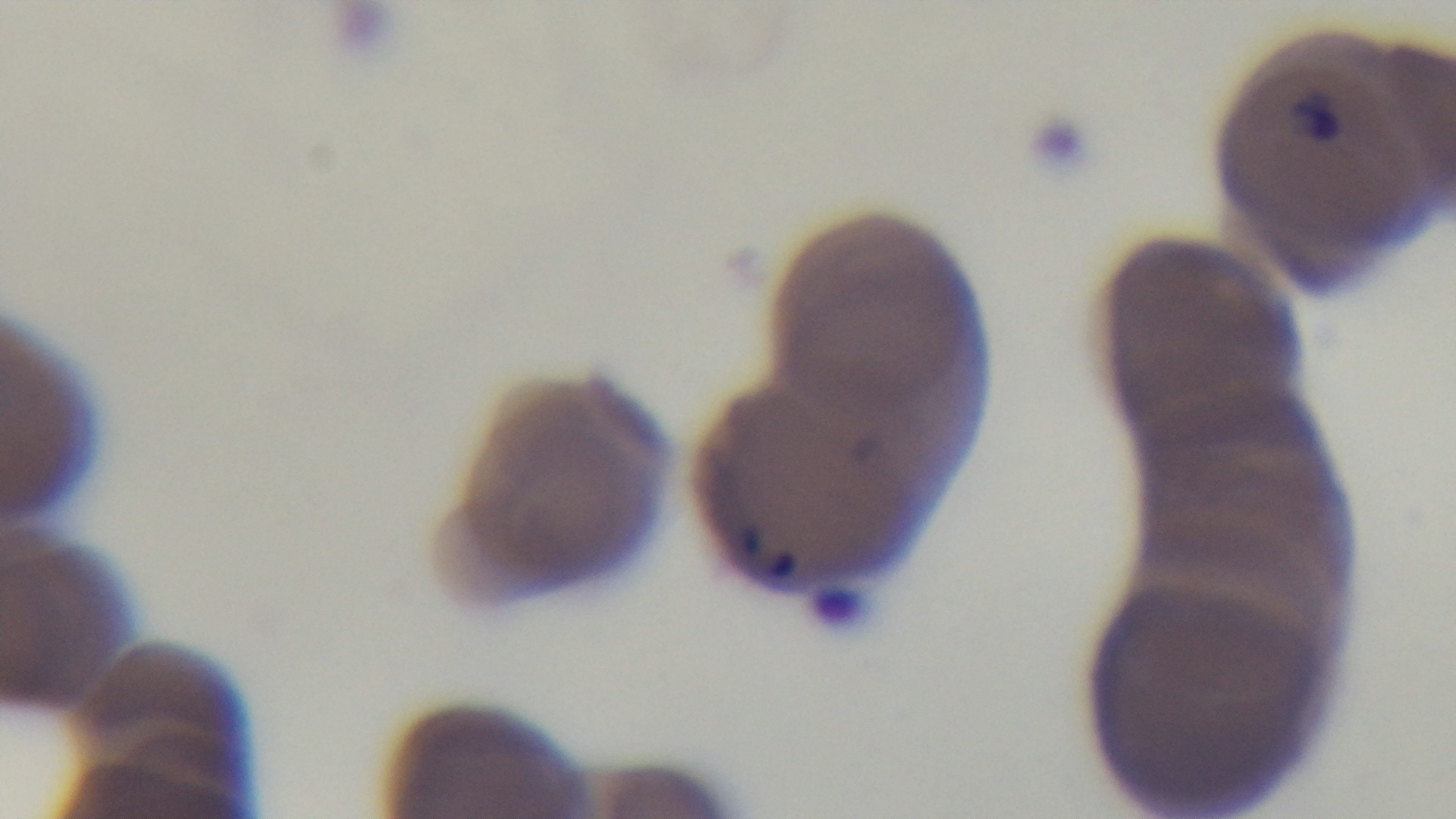

Malaria status: positive. 100x oil-immersion objective. Single field of view. Preparation: thin blood film. Light microscopy. Captured with a mounted 4K digital camera. Giemsa-stained.